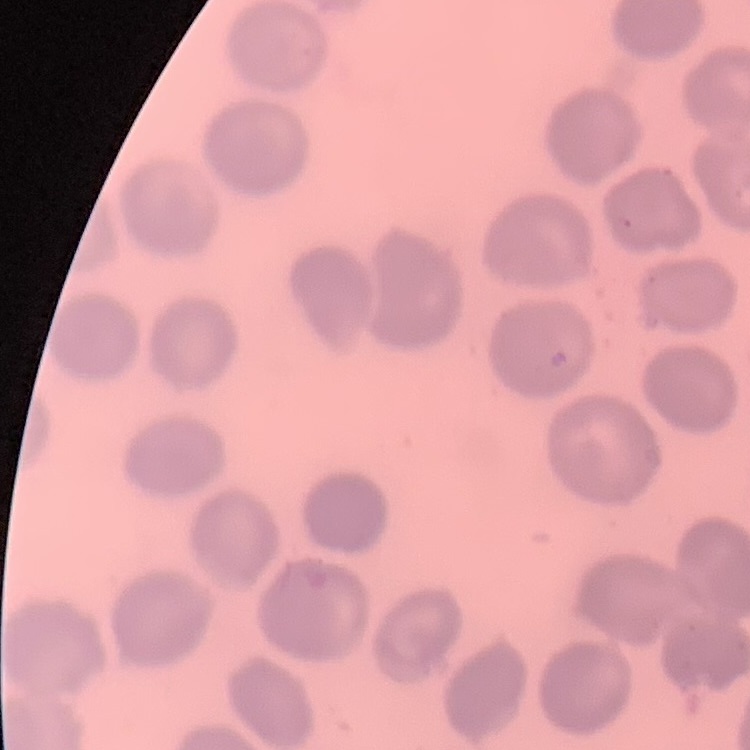
The red blood cells show no rouleaux formation. One tile cut from a larger photomicrograph. Field's or Giemsa stain. Thin blood film.